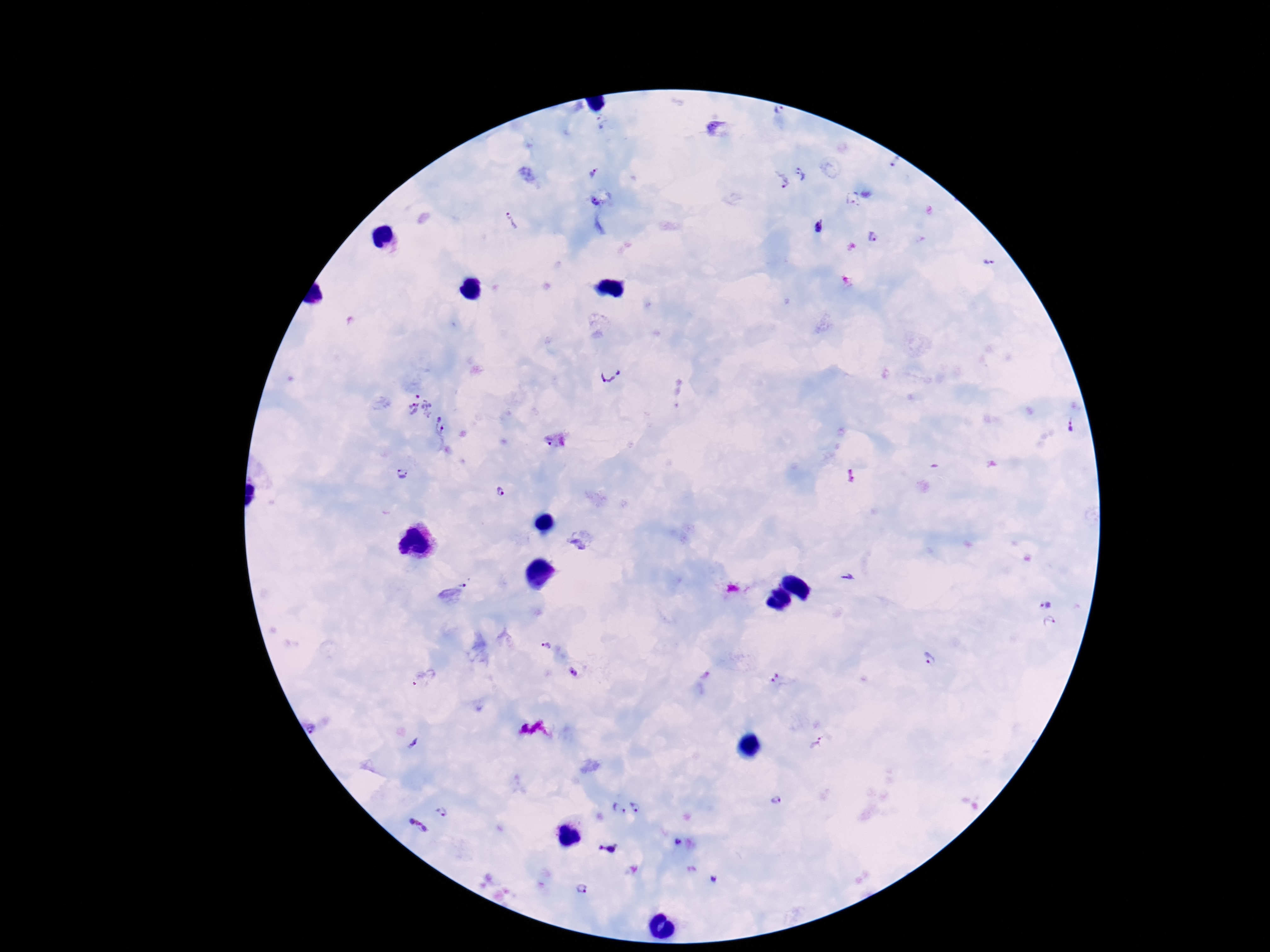

Approximate centers as {x, y} in pixels. Plasmodium parasite locations: {780, 110}, {895, 162}, {594, 173}, {803, 174}, {780, 181}, {598, 198}, {512, 223}, {817, 228}, {874, 238}, {989, 263}, {610, 369}, {419, 405}, {443, 426}, {1070, 426}, {557, 441}, {401, 474}, {503, 492}, {847, 577}, {455, 594}, {1048, 603}, {1051, 624}, {546, 645}, {930, 659}, {574, 672}, {421, 678}, {313, 727}, {818, 741}, {777, 800}, {636, 805}, {442, 810}, {618, 810}, {418, 828}, {677, 843}, {605, 847}, {712, 878}, {582, 889}. Photographed through the microscope eyepiece with a smartphone camera. Thick blood smear. Image is 1270×952 pixels. Giemsa stain. Single field of view. 100x magnification. Patient malaria status: infected.